Classify this cell by malaria status.
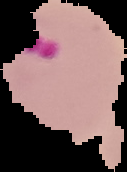
It is parasitized.

Image is 127×172 pixels. From a thin blood film. The area outside the segmented cell region is set to black.